Give the extent of all uninfected red blood cells.
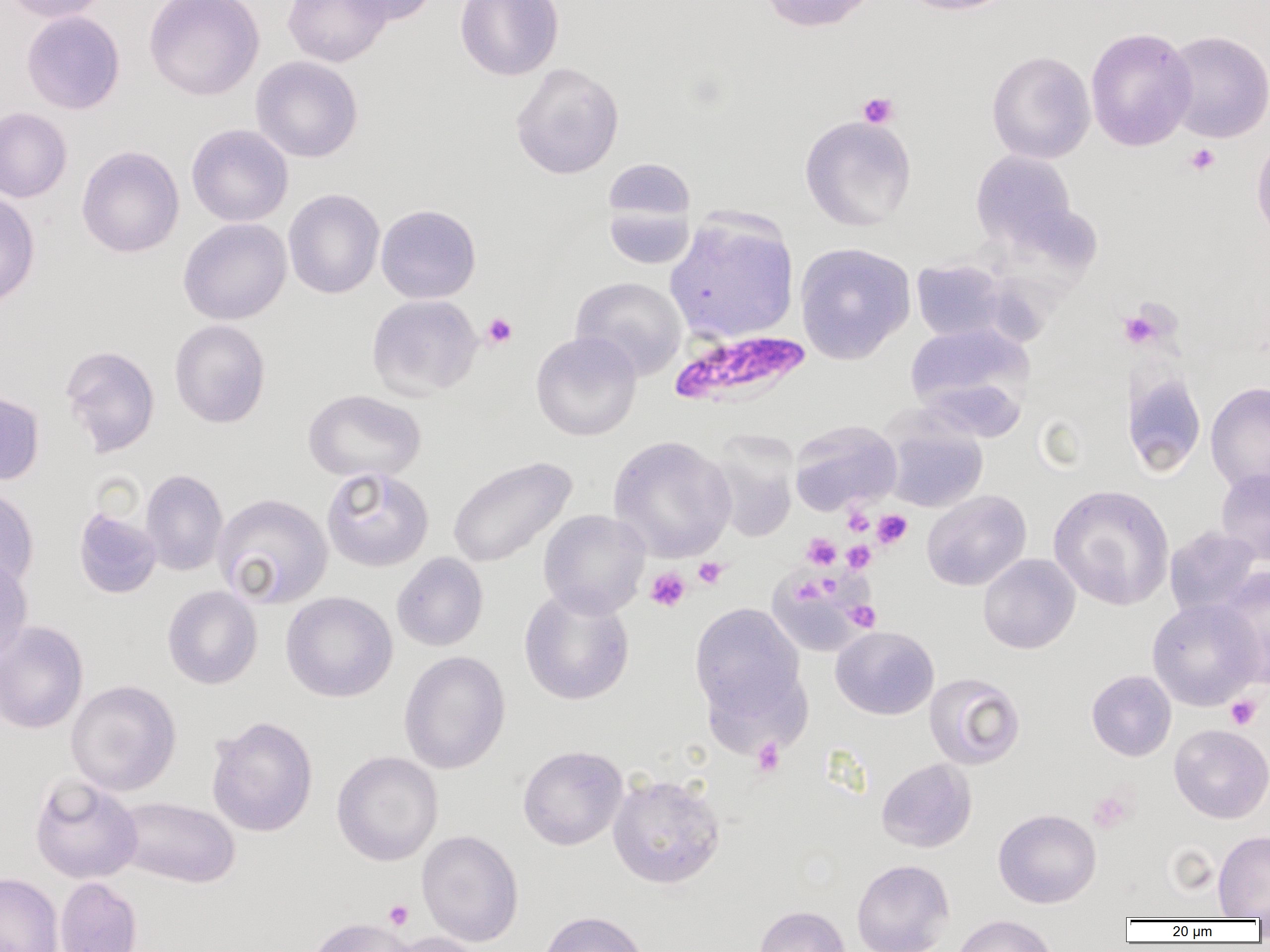

Approximate bounding boxes as [x1, y1, x2, y2] in pixels.
Uninfected red blood cells: [3, 0, 112, 23], [144, 0, 265, 101], [283, 0, 391, 67], [337, 0, 439, 25], [454, 0, 564, 81], [758, 0, 882, 33], [897, 0, 1019, 16], [21, 11, 125, 115], [1085, 27, 1197, 152], [1163, 30, 1270, 143], [986, 50, 1096, 164], [251, 56, 364, 163], [510, 61, 625, 180], [0, 107, 72, 203], [799, 115, 917, 231], [186, 124, 293, 227], [1250, 132, 1270, 244], [76, 145, 185, 258], [970, 149, 1077, 249], [603, 158, 696, 223], [283, 189, 385, 299], [0, 190, 41, 309], [603, 202, 695, 269], [375, 204, 482, 303], [664, 212, 799, 345], [178, 218, 292, 325], [794, 241, 916, 365], [911, 259, 1012, 343], [570, 276, 688, 380], [366, 294, 483, 399], [169, 319, 270, 428], [904, 321, 1035, 427], [531, 331, 642, 441], [60, 344, 160, 457], [1123, 370, 1207, 477], [1206, 382, 1270, 495], [0, 389, 45, 486], [303, 389, 427, 482], [789, 420, 902, 515], [884, 420, 988, 513], [706, 432, 800, 543], [608, 434, 737, 562], [447, 456, 577, 569], [321, 467, 434, 572], [1216, 468, 1270, 565], [140, 469, 228, 576], [0, 484, 40, 592], [1049, 484, 1175, 611], [922, 490, 1031, 591], [212, 493, 333, 609], [73, 507, 162, 599], [538, 509, 650, 618], [1164, 526, 1263, 619], [392, 552, 488, 651], [0, 553, 33, 668], [978, 553, 1080, 654], [1215, 566, 1269, 689], [769, 568, 872, 658], [162, 586, 262, 689], [518, 587, 635, 705], [281, 591, 398, 702], [1146, 598, 1263, 710], [689, 602, 806, 724], [0, 620, 89, 735], [831, 626, 939, 719], [399, 650, 510, 774], [1086, 669, 1176, 761], [924, 672, 1025, 770], [66, 679, 182, 796], [206, 715, 318, 837], [1169, 723, 1270, 823], [517, 745, 628, 850], [331, 751, 443, 866], [876, 757, 977, 853], [607, 772, 726, 889], [29, 773, 143, 883], [114, 795, 240, 889], [993, 808, 1102, 908], [416, 830, 523, 946], [1213, 830, 1270, 919], [852, 858, 954, 952], [0, 871, 63, 952], [54, 877, 142, 952], [752, 905, 851, 952], [537, 910, 650, 952], [951, 914, 1058, 952], [304, 917, 419, 952], [385, 931, 488, 952].

slide-level diagnosis = Plasmodium falciparum
modality = optical microscopy
field of view = single
Plasmodium falciparum-infected red blood cell locations = approximate bounding boxes as [x1, y1, x2, y2] in pixels: [669, 328, 812, 409]
platelet locations = approximate bounding boxes as [x1, y1, x2, y2] in pixels: [858, 92, 899, 129], [1184, 143, 1220, 176], [1120, 309, 1163, 348], [481, 312, 518, 349], [842, 505, 874, 536], [872, 509, 912, 549], [802, 533, 841, 570], [842, 541, 875, 574], [693, 558, 728, 590], [645, 567, 691, 612], [794, 577, 825, 605], [844, 600, 881, 632], [1225, 695, 1261, 730], [751, 738, 785, 777], [1088, 788, 1136, 833], [384, 900, 414, 930]
image size = 1270×952 pixels
magnification = 1000x
preparation = thin blood smear